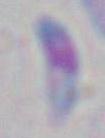

modality = micrograph
identification = Toxoplasma gondii
magnification = 1000x